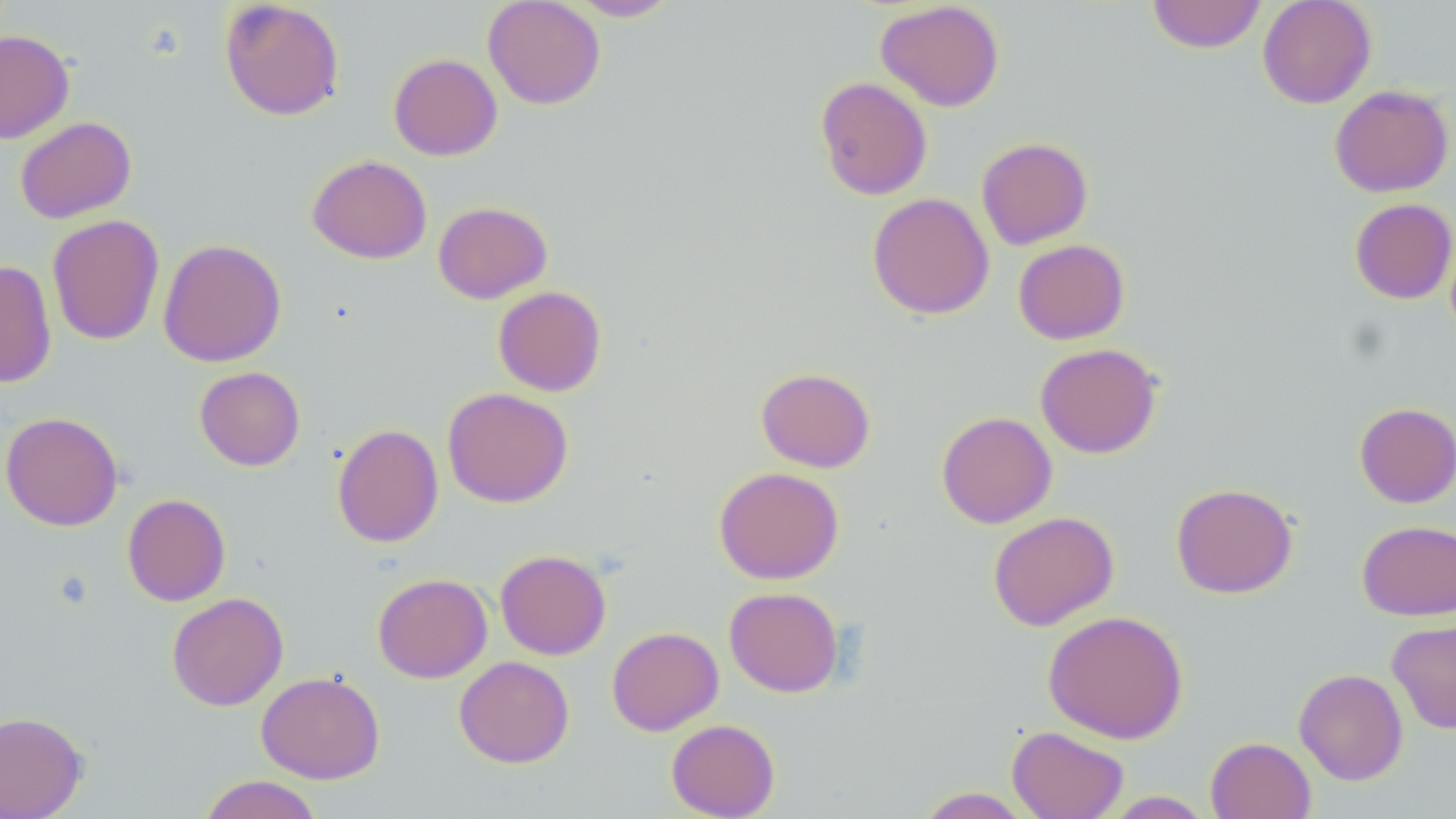
slide-level diagnosis = no evidence of blood parasites
magnification = 1000x
image size = 1456×819 pixels
modality = light microscopy
field of view = one of a larger specimen
stain = May-Grünwald-Giemsa
uninfected red blood cell locations = approximate bounding boxes as [x1, y1, x2, y2] in pixels: [219, 0, 345, 121], [482, 0, 605, 109], [567, 0, 681, 21], [1147, 0, 1267, 54], [1257, 0, 1377, 109], [875, 1, 1005, 112], [0, 30, 74, 143], [388, 53, 502, 161], [815, 76, 932, 200], [1329, 85, 1454, 198], [15, 116, 136, 223], [976, 137, 1093, 250], [307, 155, 432, 264], [867, 192, 995, 320], [1349, 198, 1456, 304], [433, 201, 552, 304], [47, 214, 164, 346], [158, 239, 286, 367], [1013, 239, 1129, 344], [0, 260, 57, 388], [493, 285, 607, 397], [1035, 343, 1162, 459], [194, 366, 305, 471], [756, 367, 876, 472], [442, 387, 573, 508], [1354, 402, 1456, 508], [0, 411, 124, 531], [936, 411, 1057, 528], [331, 423, 444, 548], [714, 466, 844, 584], [1170, 482, 1298, 599], [122, 493, 231, 606], [987, 511, 1119, 631], [1357, 520, 1456, 620], [495, 549, 611, 660], [372, 573, 492, 683], [724, 586, 844, 697], [166, 592, 288, 711], [1042, 610, 1189, 744], [1387, 619, 1456, 734], [606, 626, 724, 736], [454, 655, 575, 768], [1294, 668, 1409, 785], [256, 671, 385, 784], [0, 711, 87, 818], [666, 719, 780, 819], [1006, 725, 1129, 819], [1205, 736, 1316, 819], [198, 774, 324, 819], [913, 787, 1034, 818], [1101, 791, 1215, 818]
preparation = thin blood smear